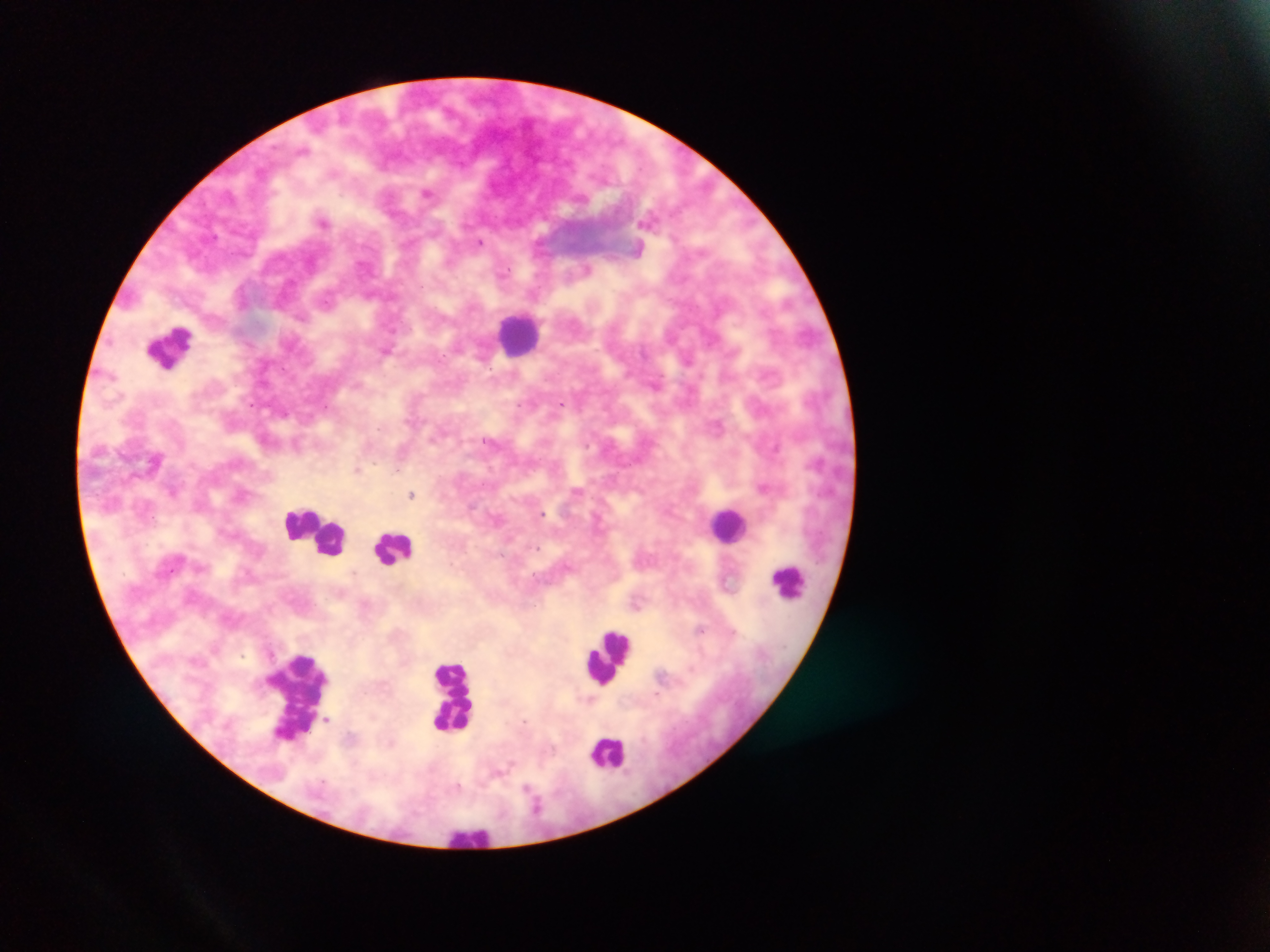 Approximate centers as (x, y) in pixels. Leukocyte locations: (520, 332), (170, 346), (728, 525), (314, 530), (393, 548), (788, 581), (609, 658), (297, 695), (453, 697), (609, 752), (470, 835). Malaria parasite locations: (428, 192), (647, 220), (324, 221), (480, 241), (638, 249), (388, 350), (561, 402), (718, 425), (357, 469), (764, 486), (173, 490), (577, 491), (412, 494), (353, 573), (638, 602), (702, 629), (327, 718). Image is 1270×952 pixels. One field of view. Mobile-phone photograph taken through the microscope. Thick blood smear. Sample from Ghana.